Assess this cell for malaria.
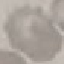

It is uninfected.

Thin blood film. Cell patch, automatically extracted from a larger field of view and resized to 64 × 64 pixels. Photographed with a smartphone camera at the microscope eyepiece. Giemsa-stained preparation.